Name the cell type shown.
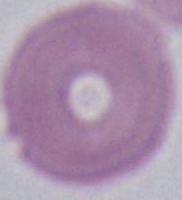
This is an erythrocyte.

Summary:
  - Magnification: 1000x
  - Modality: photomicrograph